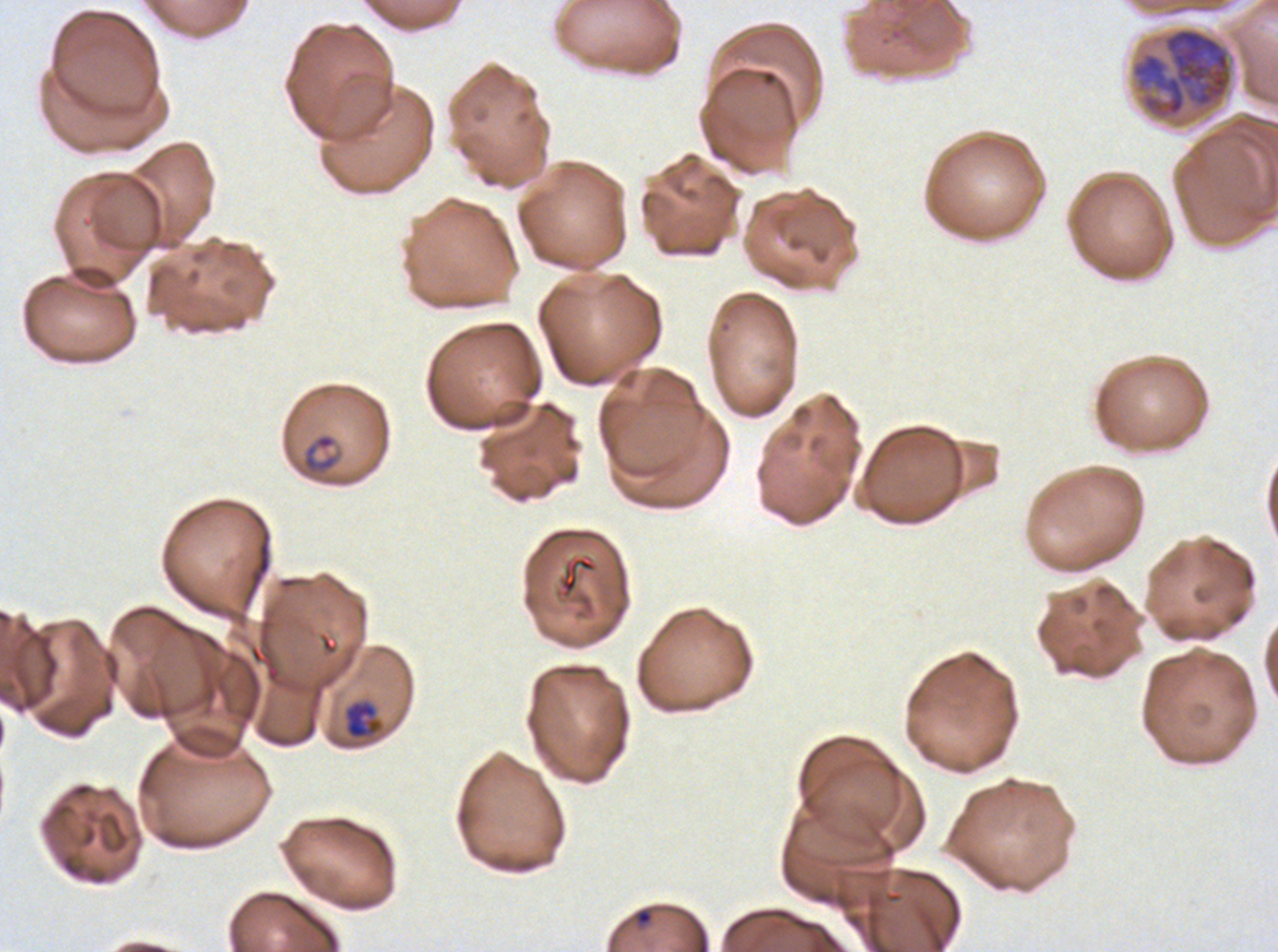 Approximate bounding boxes as [x1, y1, x2, y2] in pixels. Late-ring/early-trophozoite locations: [343, 699, 384, 740]. Early schizont locations: [1130, 26, 1234, 122]. Ring locations: [301, 433, 338, 473], [636, 909, 653, 925]. Giemsa-stained preparation. Life-cycle stages observed: ring, late-ring/early-trophozoite, early schizont. Thin blood film. Ex-vivo P. falciparum culture from a patient in The Gambia, grown for 24 to 48 hours. A sub-image separated from a larger composite. Image is 1278×952 pixels.